Classify this cell by malaria status.
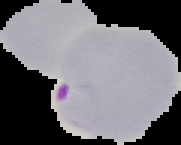
Parasitized.

image size = 181×145 pixels
image type = segmented cell region with the area outside set to black
preparation = thin blood film